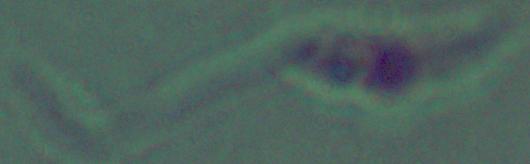

Captured at 1000x magnification. A Leishmania parasite is seen. Micrograph.